Comment on the morphology of the erythrocytes.
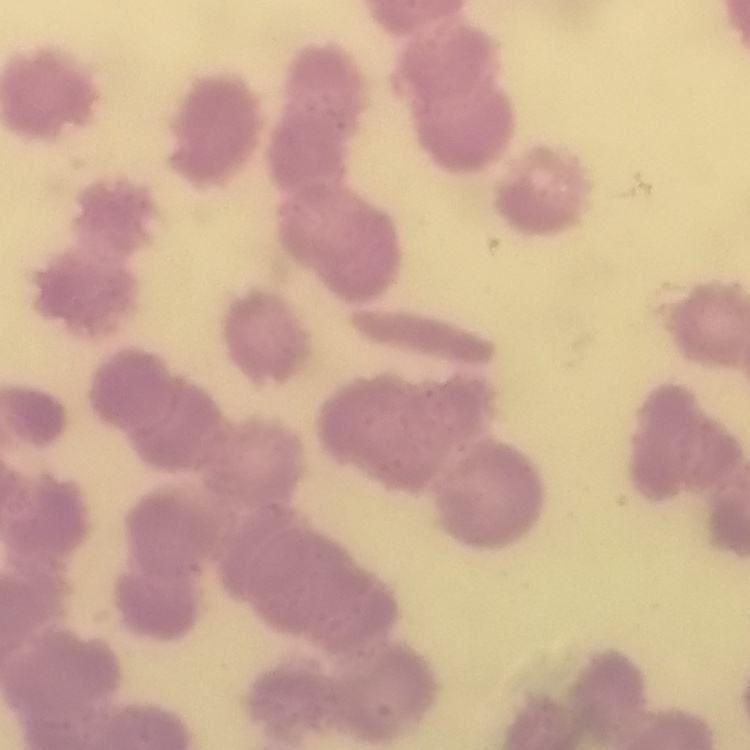

They show rouleaux formation.

Summary:
  - Preparation: thin peripheral smear
  - Image type: square crop of a larger photomicrograph
  - Stain: Field's or Giemsa